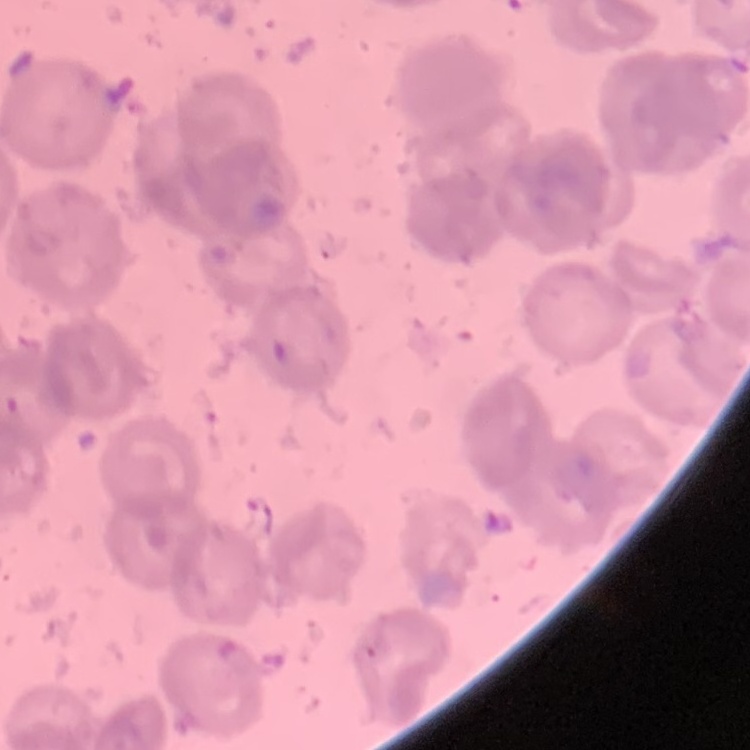 The red blood cells exhibit no rouleaux formation. One tile cut from a larger photomicrograph. Thin peripheral smear. Field's or Giemsa stain.